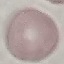

Summary:
  - Result: no malaria parasites detected
  - Preparation: thin smear
  - Stain: Giemsa
  - Image type: cell patch, automatically extracted from a larger field of view and resized to 64 × 64 pixels
  - Capture: smartphone through the microscope eyepiece